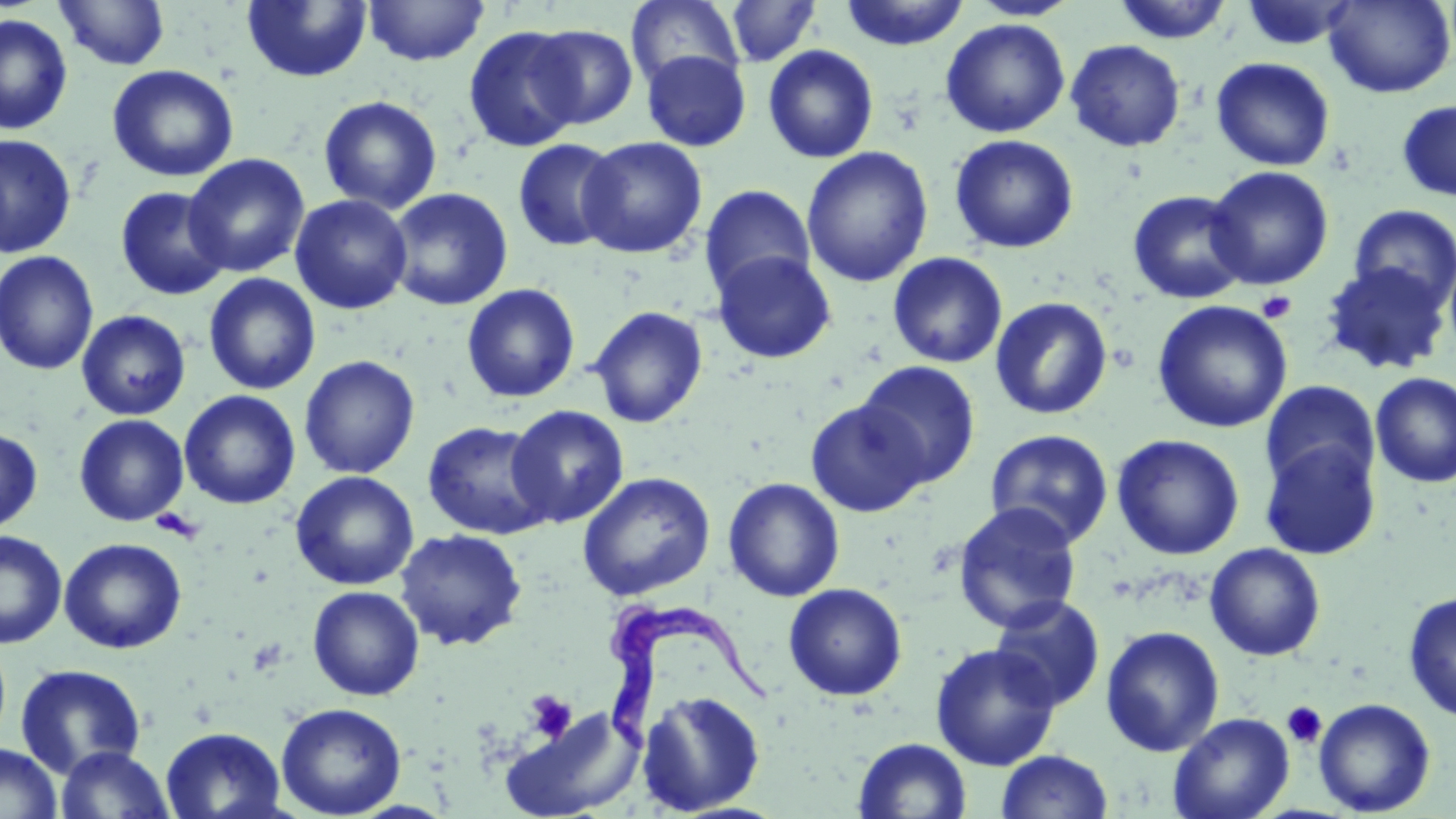

Summary:
  - Coordinate format: approximate bounding boxes as (x1, y1, x2, y2) in pixels
  - Trypanosoma brucei locations: (607, 601, 770, 757)
  - Platelet locations: (1256, 290, 1297, 324), (149, 509, 204, 543), (526, 692, 576, 742), (1282, 701, 1327, 749)
  - Uninfected red blood cell locations: (54, 0, 170, 71), (363, 0, 490, 66), (839, 0, 970, 51), (968, 0, 1080, 22), (1112, 0, 1235, 45), (1323, 0, 1456, 98), (241, 1, 373, 83), (625, 1, 745, 91), (723, 1, 822, 68), (1238, 1, 1361, 51), (0, 13, 73, 135), (940, 18, 1070, 138), (463, 25, 584, 152), (527, 25, 639, 129), (1065, 40, 1186, 152), (762, 44, 879, 164), (641, 50, 751, 151), (1211, 56, 1335, 172), (106, 64, 239, 182), (318, 95, 442, 214), (1396, 100, 1456, 202), (0, 134, 77, 258), (948, 134, 1080, 254), (577, 136, 707, 259), (513, 138, 623, 252), (801, 146, 934, 288), (183, 153, 310, 278), (1205, 165, 1334, 290), (699, 185, 816, 300), (114, 186, 231, 300), (385, 187, 514, 311), (1127, 189, 1251, 305), (290, 194, 413, 315), (1348, 204, 1456, 314), (712, 250, 837, 364), (0, 251, 99, 376), (887, 252, 1008, 369), (1320, 262, 1452, 376), (203, 273, 321, 395), (461, 283, 581, 403), (990, 296, 1113, 420), (1152, 300, 1293, 434), (588, 306, 708, 428), (76, 310, 191, 421), (299, 355, 420, 478), (855, 361, 981, 489), (1370, 372, 1456, 488), (1259, 380, 1380, 495), (179, 390, 301, 510), (805, 399, 928, 517), (506, 405, 629, 528), (74, 414, 189, 526), (422, 421, 553, 540), (0, 426, 43, 534), (985, 429, 1114, 548), (1111, 433, 1245, 560), (1259, 440, 1382, 560), (290, 470, 419, 590), (577, 472, 716, 601), (723, 477, 845, 602), (952, 502, 1083, 633), (394, 529, 527, 651), (0, 531, 67, 648), (59, 537, 187, 654), (1204, 542, 1326, 661), (783, 582, 907, 701), (307, 585, 425, 701), (1403, 591, 1456, 723), (989, 595, 1105, 711), (1100, 625, 1225, 757), (930, 643, 1061, 770), (14, 663, 147, 779), (637, 690, 766, 815), (1314, 697, 1436, 816), (275, 702, 407, 818), (502, 707, 644, 818), (1168, 711, 1294, 819), (161, 726, 287, 819), (852, 736, 973, 819), (0, 742, 62, 819), (55, 745, 175, 818), (995, 749, 1114, 818)
  - Slide-level diagnosis: Trypanosoma brucei
  - Field of view: one of a larger specimen
  - Preparation: thin blood smear
  - Image size: 1456×819 pixels
  - Magnification: 1000x
  - Modality: light microscopy
  - Stain: May-Grünwald-Giemsa